Classify this cell by malaria status.
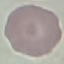
It is uninfected.

Acquired by smartphone through the microscope eyepiece. Thin smear of blood. Giemsa-stained preparation. Cell patch, automatically extracted from a larger field of view and resized to 64 × 64 pixels.